Classify this cell by malaria status.
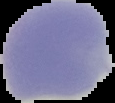

It is uninfected.

image_type: segmented cell region with the area outside set to black
preparation: thin blood film
image_size: 115×103 pixels